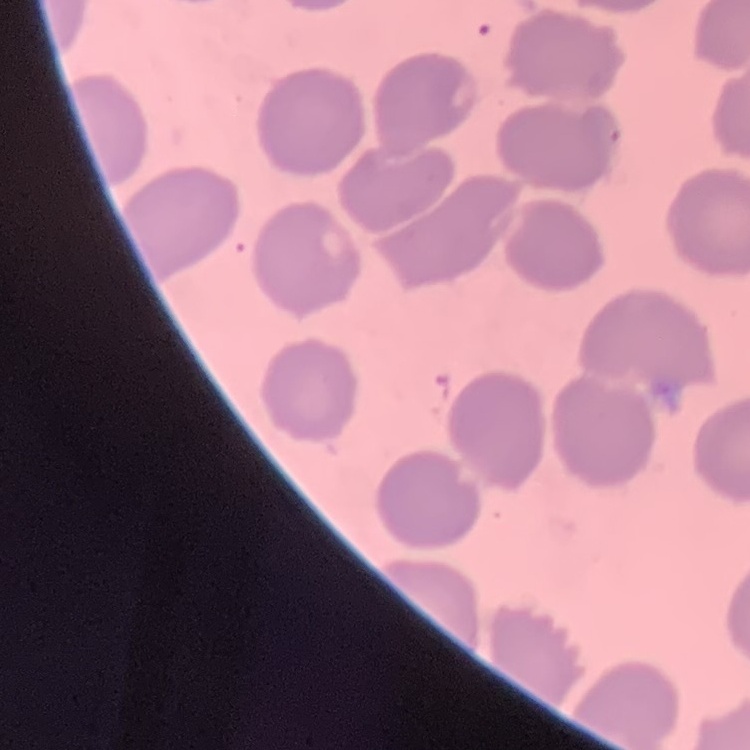

The red blood cells show no rouleaux formation. Field's or Giemsa stain. Thin blood film. One tile cut from a larger photomicrograph.